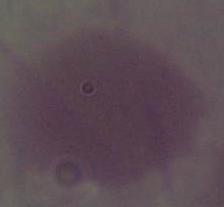

Summary:
  - Modality: photomicrograph
  - Identification: erythrocyte
  - Magnification: 1000x